Point out each malaria parasite.
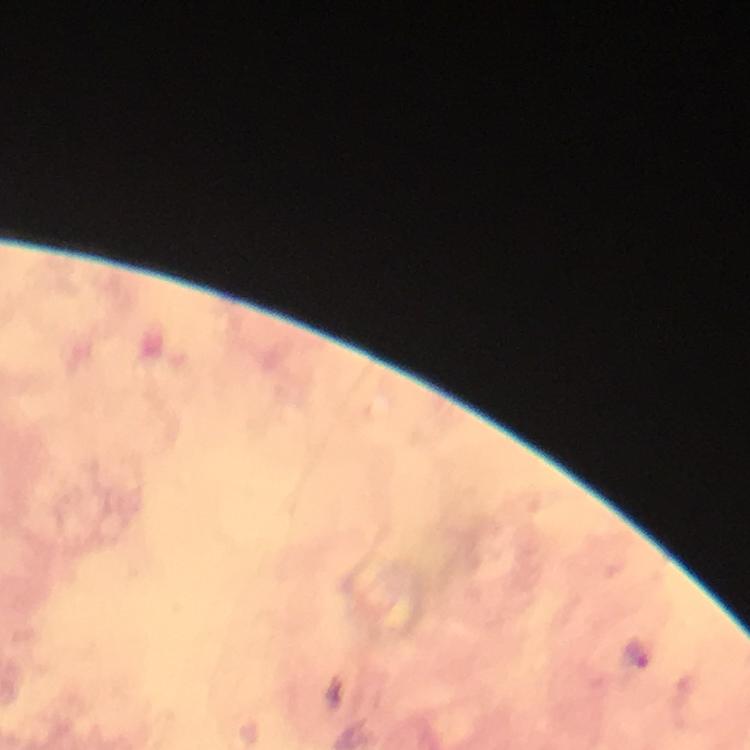
Approximate centers as [x, y] in pixels.
Malaria parasites: [637, 655].

Summary:
  - Preparation: thick blood smear
  - Cropped from: a single field of view
  - Capture: smartphone mounted on the microscope
  - Context: from a diagnostic examination for malaria
  - Image size: 750×750 pixels
  - Immersion oil: used
  - Stain: Giemsa
  - Magnification: 100x